Describe the morphology of the red blood cells.
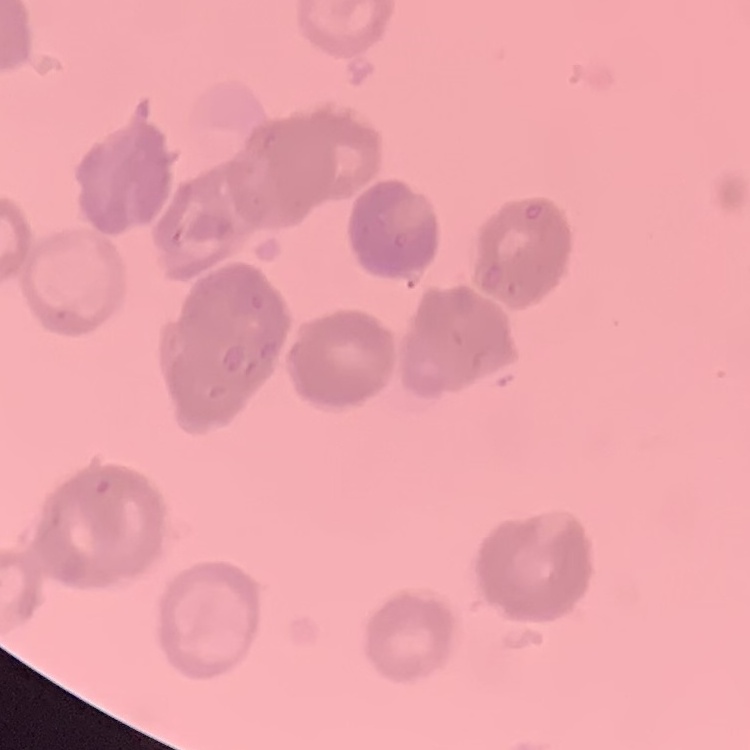

They show rouleaux formation.

Summary:
  - Preparation: thin blood film
  - Stain: Field's or Giemsa
  - Image type: square crop of a larger photomicrograph